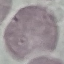
{
  "malaria_status": "uninfected",
  "preparation": "thin smear",
  "capture": "smartphone through the microscope eyepiece",
  "stain": "Giemsa",
  "image_type": "automatically extracted cell patch, resized to 64 × 64 pixels"
}